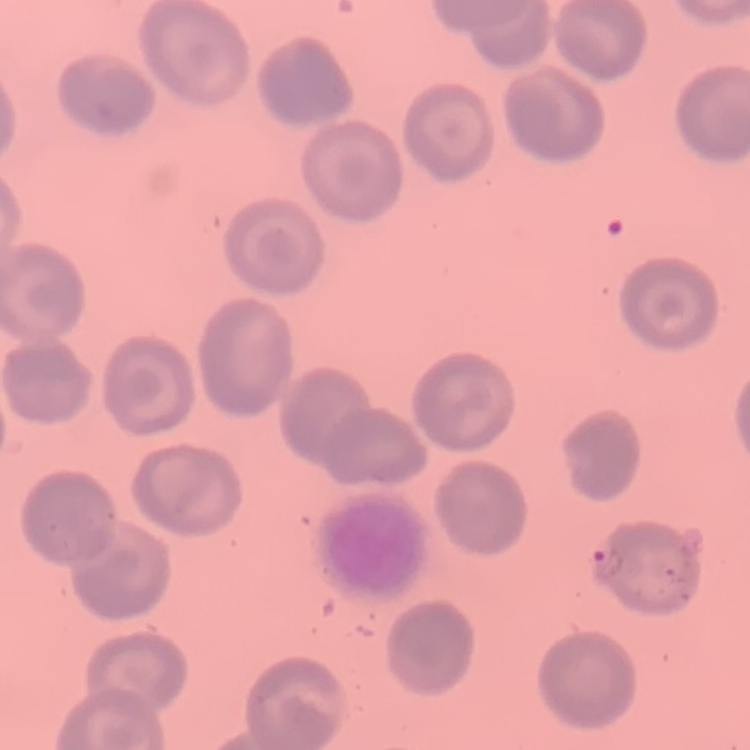
The red blood cells exhibit no rouleaux formation. Stained with either Field's or Giemsa. Thin blood film. One tile cut from a larger photomicrograph.